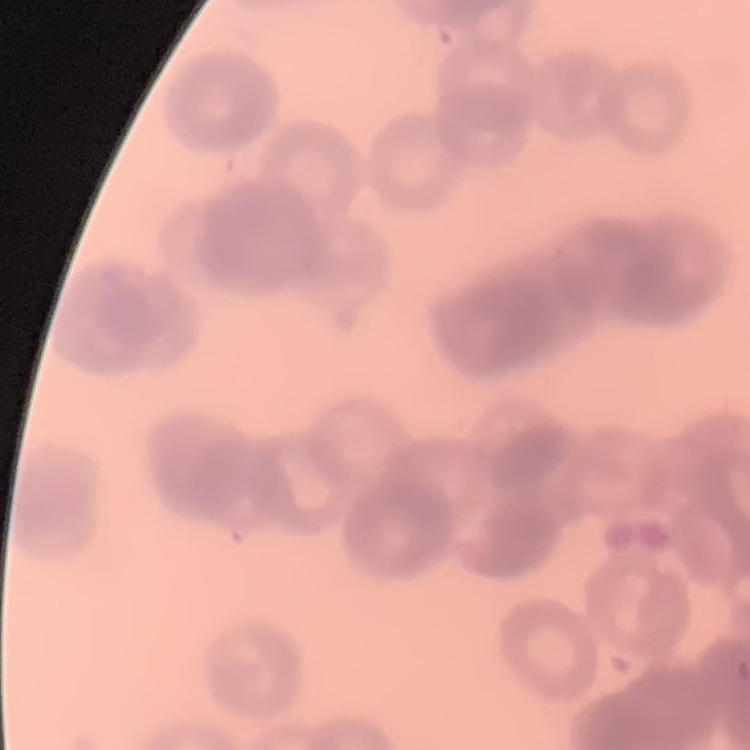
{
  "red_blood_cell_morphology": "rouleaux formation",
  "stain": "Field's or Giemsa",
  "image_type": "one tile cut from a larger photomicrograph",
  "preparation": "thin peripheral smear"
}